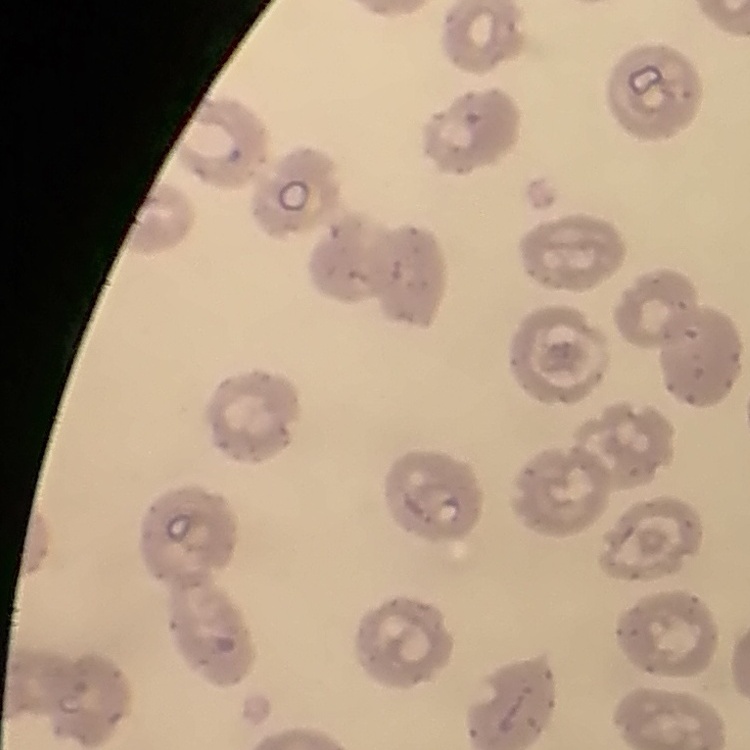

red blood cell morphology = no rouleaux formation
stain = Field's or Giemsa
preparation = thin blood film
image type = square crop of a larger photomicrograph